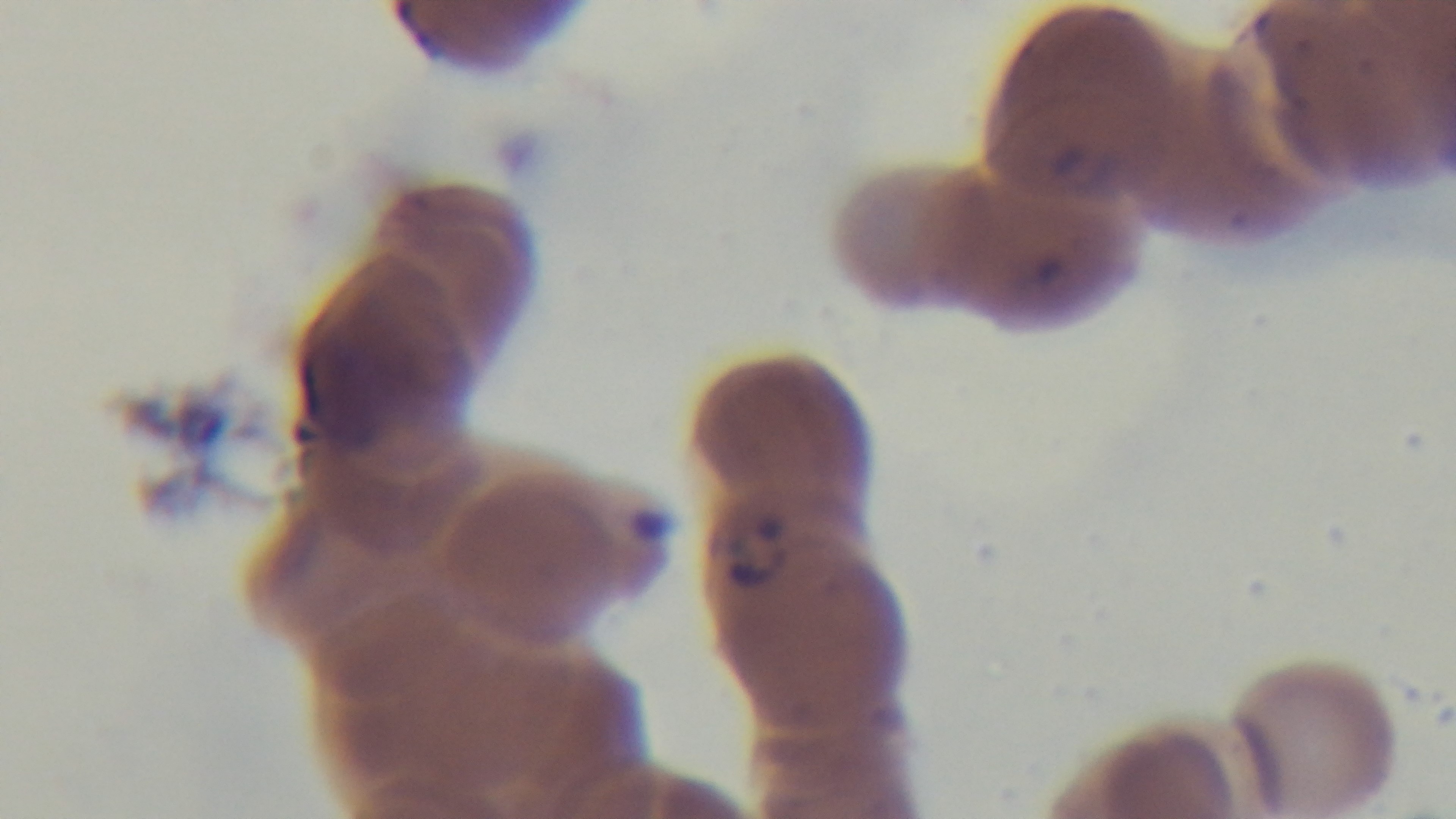

Summary:
  - Malaria status: infected
  - Modality: light microscopy
  - Stain: Giemsa
  - Field of view: single
  - Objective: 100x oil immersion
  - Preparation: thin
  - Capture: mounted 4K digital camera